Give the position of every Plasmodium parasite, noting whether each is a trophozoite, schizont, or gametocyte.
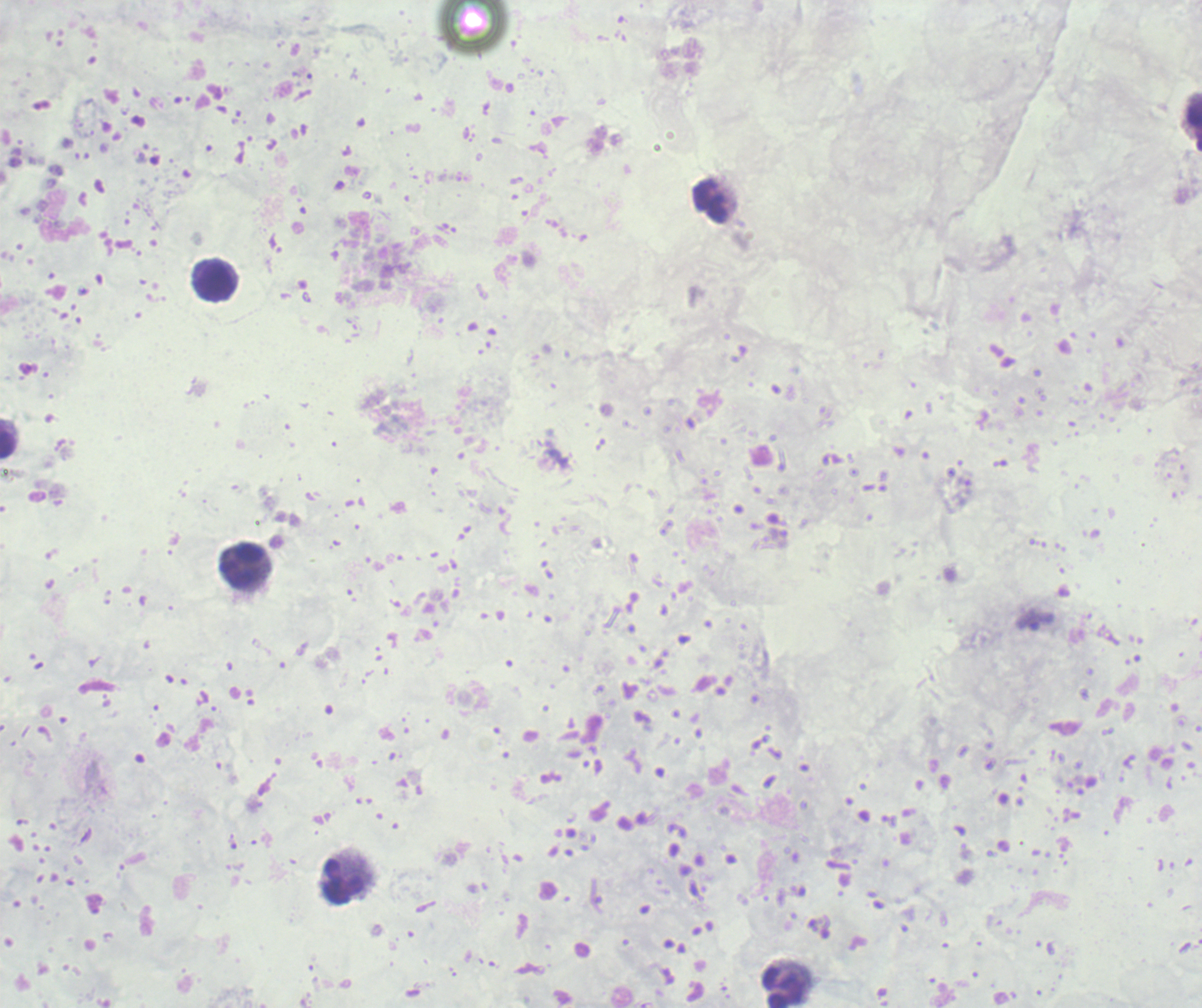
Negative for Plasmodium parasites.

Approximate centers as [x, y] in pixels. Leukocyte locations: [1195, 126], [711, 201], [214, 280], [9, 439], [243, 566], [344, 880], [784, 988]. Previously used in a real diagnosis. Romanowsky-stained preparation. 100x magnification. Single field of view. Thick blood film. Image is 1202×1008 pixels. Background quality: unsatisfactory.